Give the position of every Plasmodium parasite.
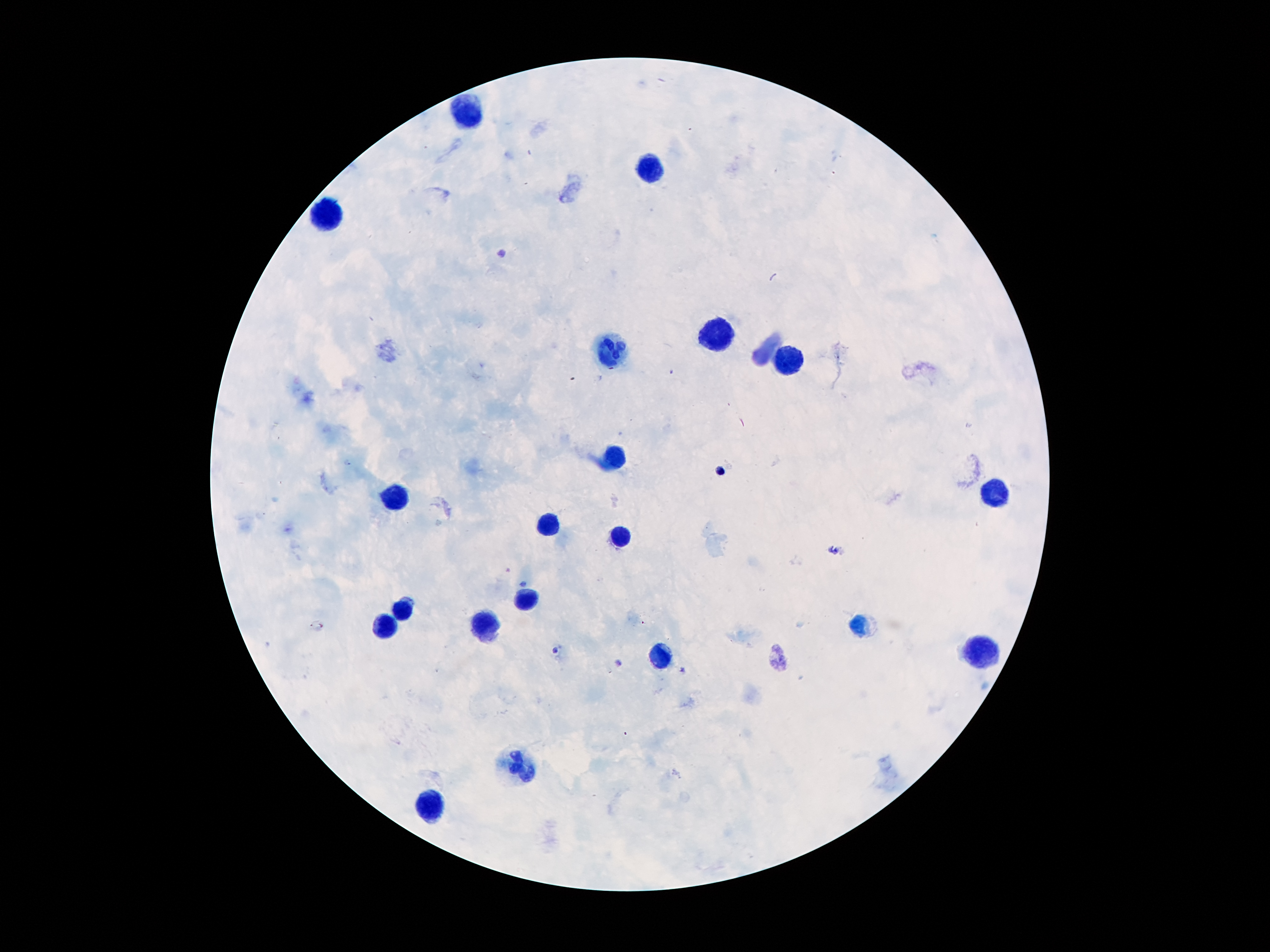
Approximate object centers, in pixels from the top-left corner.
Plasmodium parasites: (x=720, y=472), (x=523, y=582), (x=555, y=650), (x=619, y=664).

Summary:
  - Leukocyte locations: (x=471, y=112), (x=651, y=166), (x=328, y=214), (x=716, y=338), (x=615, y=353), (x=787, y=359), (x=612, y=458), (x=996, y=493), (x=395, y=499), (x=549, y=524), (x=620, y=535), (x=526, y=598), (x=404, y=610), (x=385, y=626), (x=486, y=629), (x=983, y=654), (x=659, y=656), (x=518, y=766), (x=430, y=805)
  - Capture: smartphone through the microscope eyepiece
  - Field of view: one from this slide
  - Preparation: thick blood film
  - Image size: 1270×952 pixels
  - Stain: Giemsa
  - Patient malaria status: positive for Plasmodium falciparum
  - Magnification: 100x